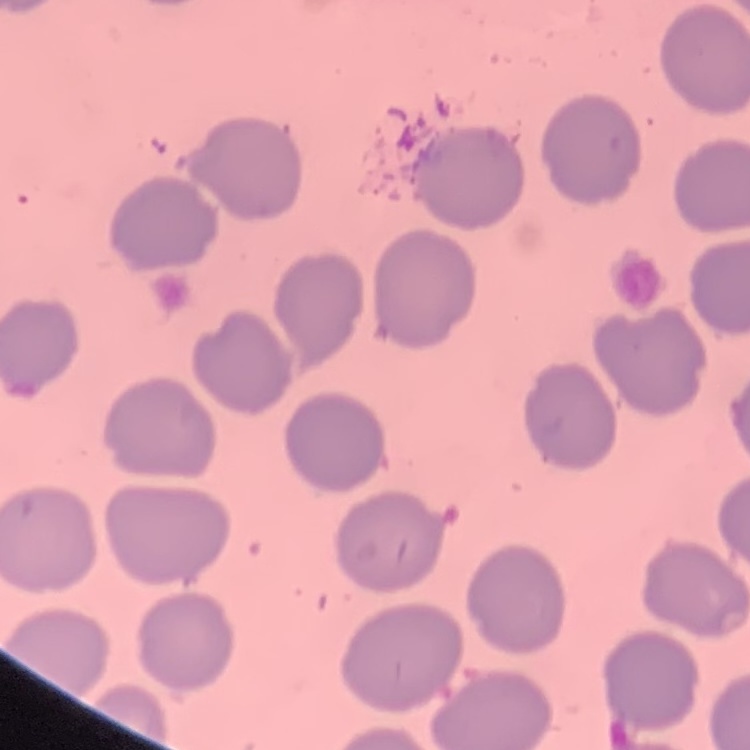 The erythrocytes exhibit no rouleaux formation. Stained with either Field's or Giemsa. Thin blood film. Square crop of a larger photomicrograph.